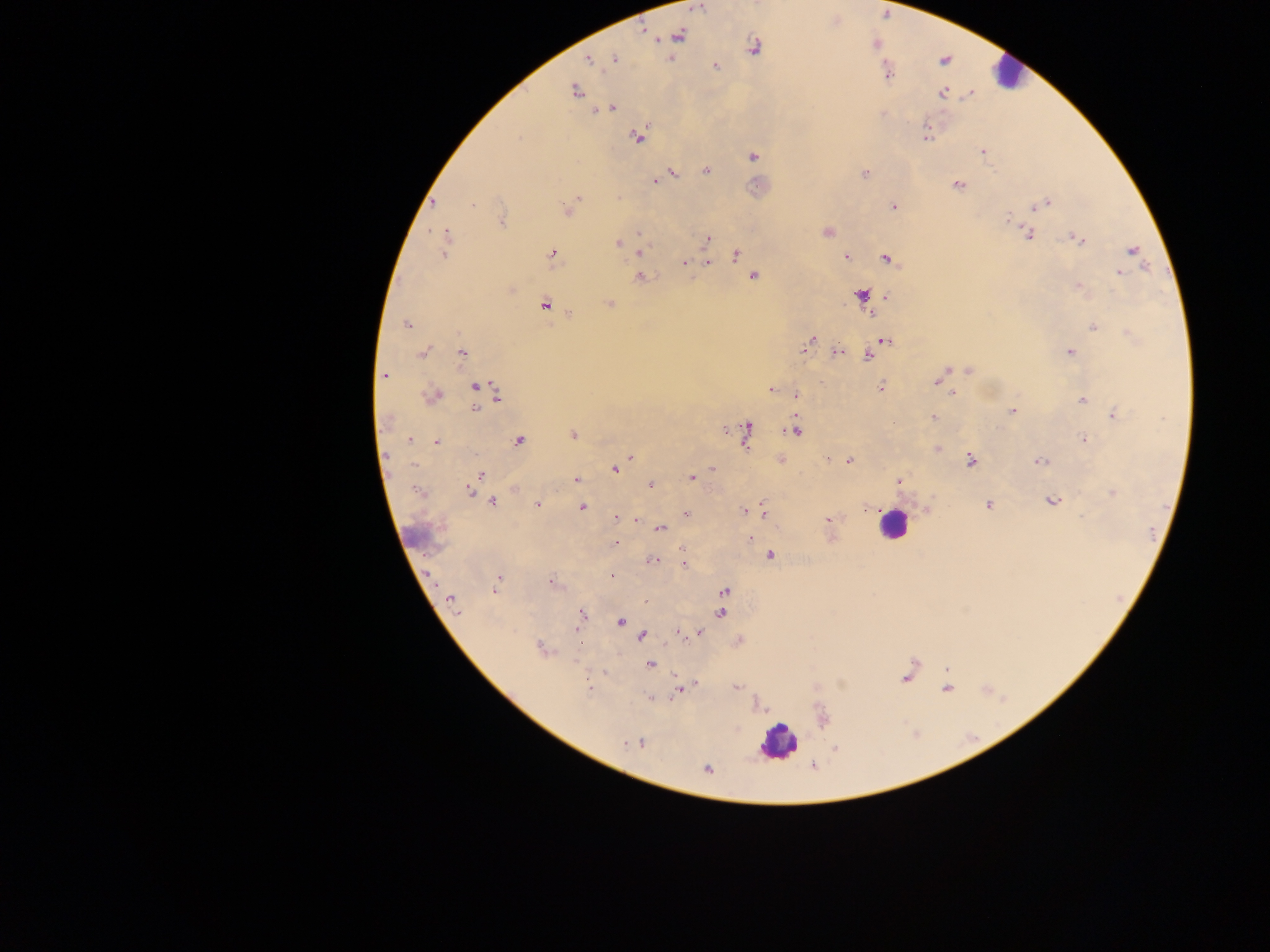 Approximate centers as (x, y) in pixels. Malaria parasite locations: (698, 8), (680, 36), (753, 48), (615, 59), (589, 60), (715, 65), (887, 72), (575, 91), (942, 94), (611, 108), (603, 112), (926, 134), (638, 136), (983, 152), (753, 157), (706, 170), (673, 173), (864, 174), (655, 181), (957, 185), (577, 199), (434, 203), (1045, 204), (472, 205), (893, 207), (568, 209), (1008, 218), (502, 221), (827, 232), (446, 233), (639, 233), (1028, 235), (707, 239), (1078, 239), (444, 242), (617, 243), (639, 249), (1132, 251), (444, 254), (553, 254), (736, 255), (846, 256), (886, 258), (684, 263), (707, 263), (1119, 272), (639, 277), (752, 277), (1078, 287), (860, 295), (886, 296), (608, 304), (545, 305), (407, 324), (1093, 326), (885, 341), (809, 343), (1070, 352), (423, 353), (838, 353), (462, 354), (868, 355), (948, 370), (968, 371), (385, 376), (937, 382), (476, 387), (479, 388), (880, 388), (771, 389), (497, 393), (951, 393), (433, 397), (796, 397), (1082, 400), (475, 410), (1013, 410), (1115, 415), (932, 417), (725, 430), (796, 430), (746, 431), (573, 435), (1083, 439), (410, 440), (519, 441), (436, 443), (938, 449), (630, 457), (780, 460), (848, 461), (971, 461), (1040, 461), (713, 468), (615, 469), (481, 475), (691, 477), (476, 479), (576, 480), (899, 481), (651, 485), (514, 488), (470, 491), (1113, 493), (1052, 500), (492, 502), (538, 504), (989, 505), (583, 508), (763, 510), (744, 511), (685, 513), (616, 517), (1082, 517), (829, 519), (636, 521), (661, 530), (750, 539), (616, 543), (770, 556), (652, 562), (685, 563), (611, 576), (550, 582), (496, 586), (726, 592), (451, 600), (646, 601), (455, 611), (721, 613), (582, 614), (621, 621), (576, 629), (677, 632), (699, 633), (642, 635), (542, 649), (650, 664), (947, 668), (604, 673), (906, 678), (692, 685), (588, 686), (736, 687), (681, 689), (947, 689), (652, 698), (641, 743), (626, 745), (836, 747), (708, 769). Leukocyte locations: (1008, 74), (892, 524), (409, 537), (777, 742). Sample from Ghana. Image is 1270×952 pixels. One field of view. Photographed through a microscope with a mobile-phone camera. Thick blood smear.